Point out each Plasmodium parasite.
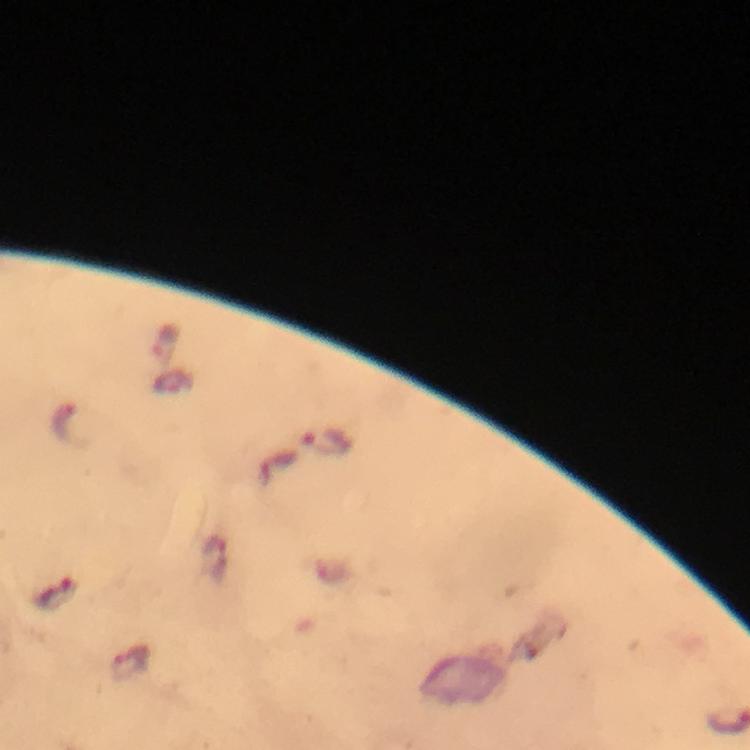

Approximate centers as (x, y) in pixels.
Plasmodium parasites: (326, 442), (54, 594), (131, 662).

Summary:
  - Image size: 750×750 pixels
  - Immersion oil: used
  - Capture: smartphone camera through the microscope
  - Preparation: thick blood smear
  - Stain: Giemsa
  - Context: from a malaria diagnostic workup
  - Cropped from: one field of view
  - Magnification: 100x